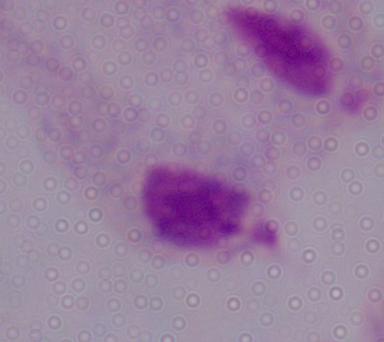

Summary:
  - Magnification: 1000x
  - Modality: photomicrograph
  - Identification: trichomonad